Comment on the morphology of the red blood cells.
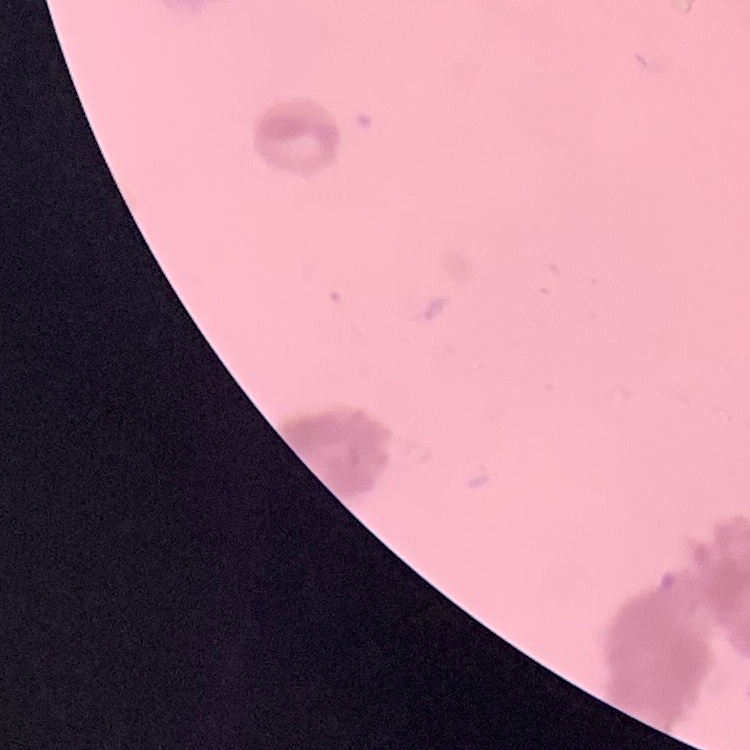
They show rouleaux formation.

image type = square crop of a larger photomicrograph
preparation = thin blood film
stain = Field's or Giemsa